Report the malaria status of this cell.
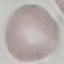

It is uninfected.

image type = cell patch, automatically extracted from a larger field of view and resized to 64 × 64 pixels
capture = smartphone through the microscope eyepiece
preparation = thin smear
stain = Giemsa